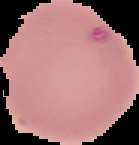

malaria status = parasitized
preparation = thin blood smear
image type = segmented cell region with the area outside set to black
image size = 139×145 pixels